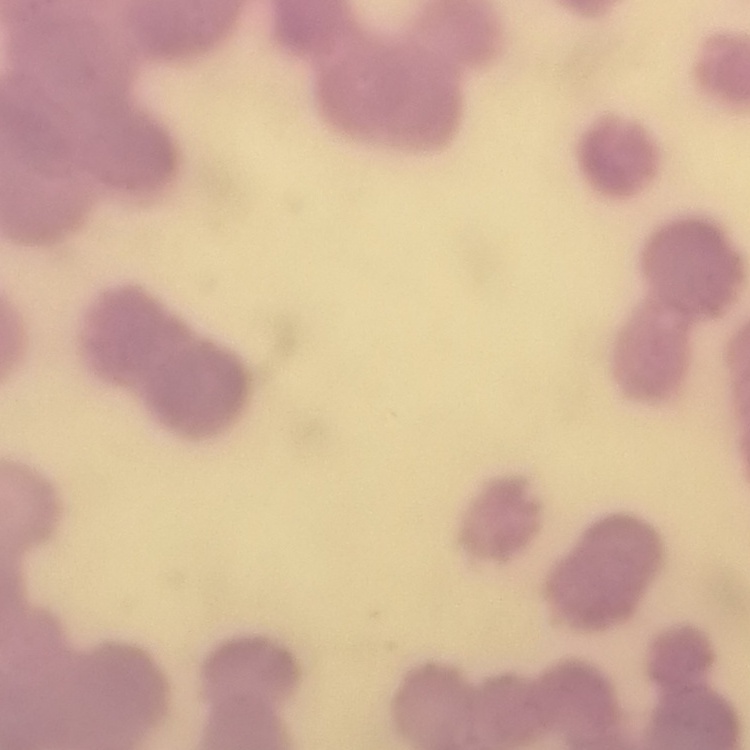

Summary:
  - Red blood cell morphology: rouleaux formation
  - Preparation: thin blood smear
  - Image type: square crop of a larger photomicrograph
  - Stain: Field's or Giemsa